State the blood parasite species.
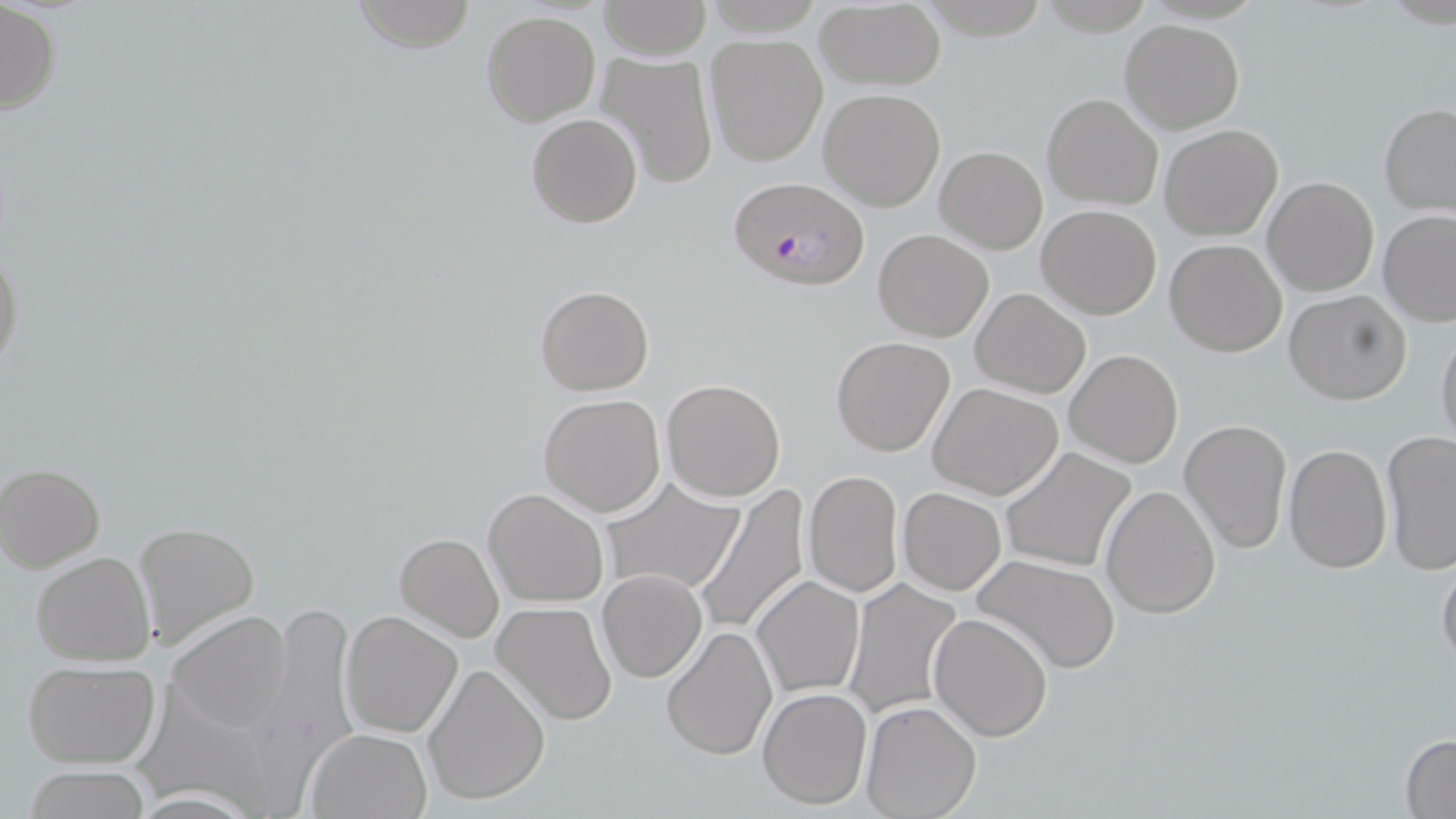
Plasmodium falciparum.

Summary:
  - Coordinate format: approximate bounding boxes as (x1, y1, x2, y2) in pixels
  - Uninfected red blood cell locations: (351, 0, 477, 52), (599, 0, 711, 60), (1, 1, 63, 118), (814, 3, 946, 90), (481, 10, 602, 126), (1120, 19, 1244, 134), (704, 35, 828, 167), (591, 51, 718, 189), (818, 88, 946, 211), (1041, 92, 1163, 210), (1379, 102, 1456, 218), (525, 112, 642, 228), (1160, 125, 1283, 240), (935, 144, 1048, 254), (1263, 176, 1378, 296), (1037, 204, 1162, 319), (1376, 210, 1456, 327), (873, 228, 993, 342), (1165, 239, 1288, 356), (0, 241, 24, 380), (535, 284, 653, 396), (969, 285, 1090, 397), (1284, 289, 1411, 405), (1436, 324, 1456, 454), (831, 335, 956, 457), (1065, 348, 1184, 468), (660, 379, 786, 502), (928, 383, 1062, 500), (538, 393, 666, 517), (1178, 418, 1291, 555), (1380, 430, 1456, 574), (1283, 443, 1391, 573), (1000, 446, 1137, 572), (1, 464, 105, 572), (802, 470, 904, 598), (601, 478, 744, 599), (1099, 483, 1219, 620), (690, 484, 812, 638), (898, 487, 1005, 595), (483, 488, 609, 607), (134, 521, 259, 654), (394, 532, 503, 641), (30, 550, 156, 667), (973, 553, 1121, 674), (1437, 554, 1456, 669), (597, 569, 706, 682), (752, 575, 865, 699), (843, 580, 964, 722), (491, 601, 618, 728), (340, 608, 463, 737), (167, 609, 294, 734), (929, 612, 1053, 741), (661, 625, 777, 760), (22, 661, 161, 769), (422, 661, 549, 806), (758, 687, 872, 811), (860, 700, 982, 818), (306, 727, 434, 818), (1399, 734, 1456, 817), (21, 764, 153, 819)
  - Plasmodium falciparum-infected red blood cell locations: (726, 177, 870, 292)
  - Magnification: 1000x
  - Image size: 1456×819 pixels
  - Stain: May-Grünwald-Giemsa
  - Modality: optical microscopy
  - Preparation: thin blood smear
  - Field of view: single